Comment on the morphology of the erythrocytes.
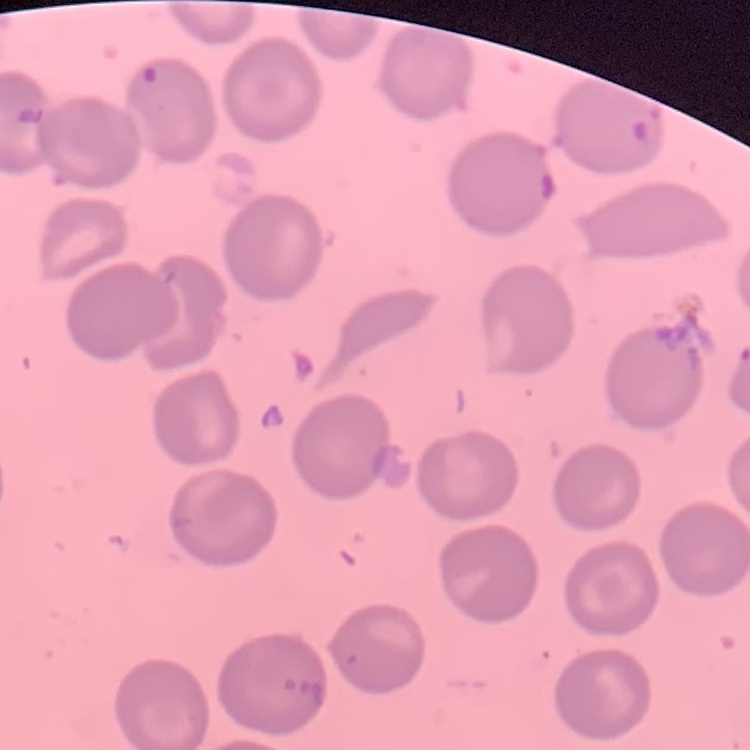

No rouleaux formation.

stain = Field's or Giemsa
preparation = thin blood smear
image type = square crop of a larger photomicrograph